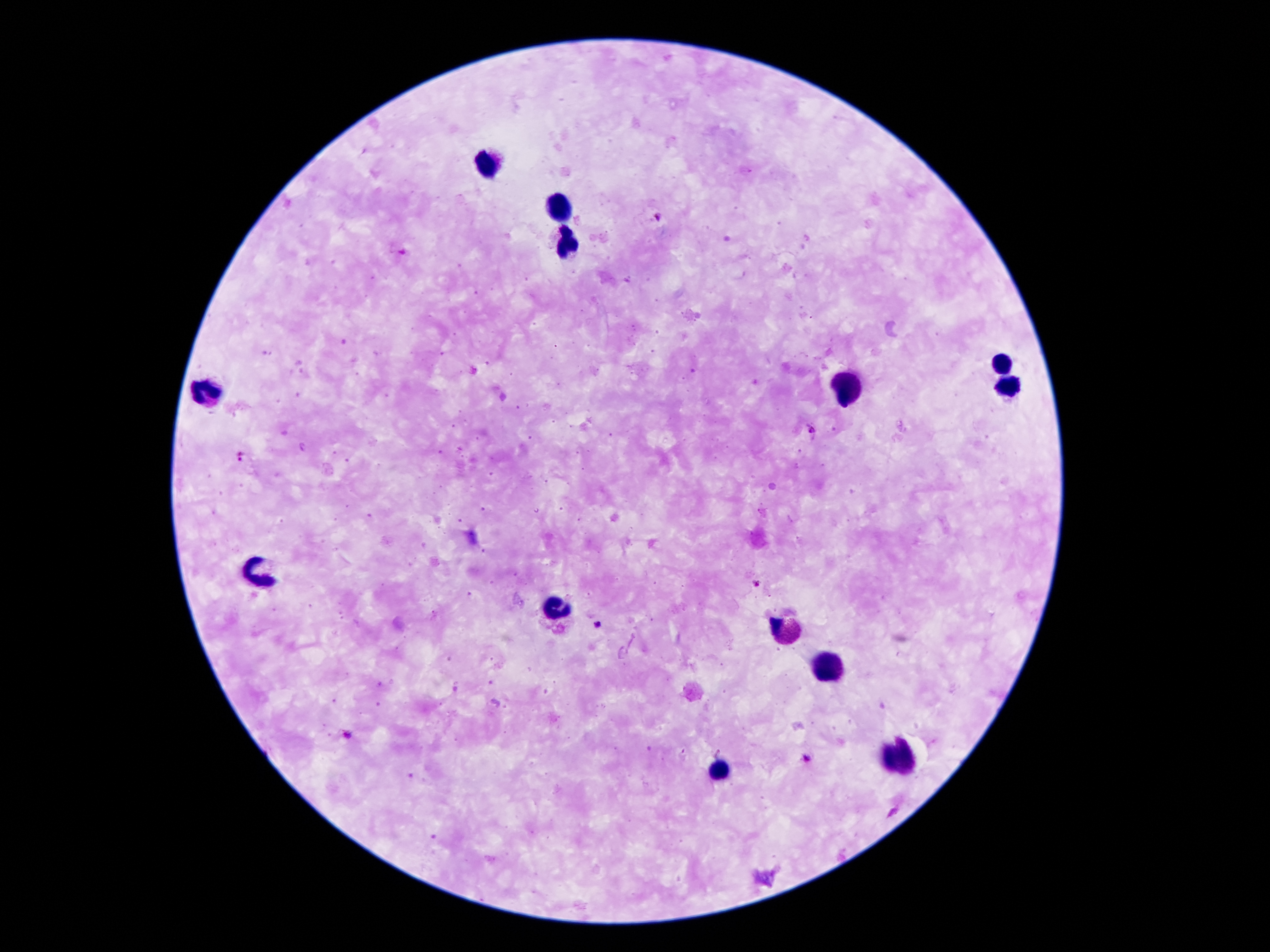
Approximate object centers, in pixels from the top-left corner.
Summary:
  - Leukocyte locations: (x=489, y=165), (x=559, y=212), (x=565, y=246), (x=1000, y=364), (x=846, y=388), (x=1008, y=388), (x=208, y=390), (x=258, y=569), (x=557, y=604), (x=785, y=630), (x=830, y=668), (x=899, y=758), (x=720, y=771)
  - Malaria parasite locations: (x=657, y=218), (x=812, y=429), (x=241, y=456), (x=757, y=584), (x=597, y=623), (x=347, y=733), (x=806, y=759)
  - Field of view: one from this slide
  - Capture: smartphone camera through the microscope eyepiece
  - Patient malaria status: positive for Plasmodium falciparum
  - Stain: Giemsa
  - Magnification: 100x
  - Preparation: thick blood film
  - Image size: 1270×952 pixels